Comment on the morphology of the erythrocytes.
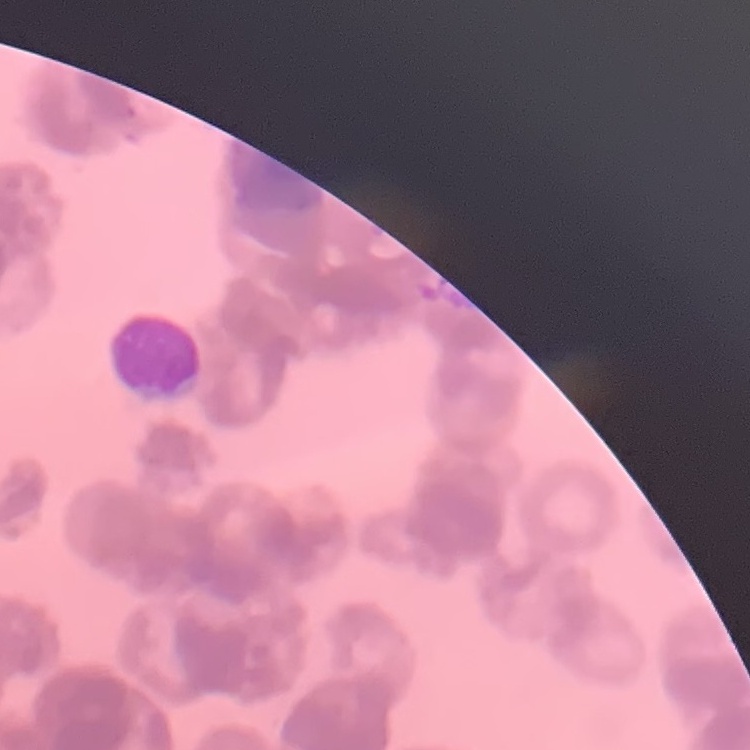
Rouleaux formation.

Square crop of a larger photomicrograph. Stained with either Field's or Giemsa. Thin peripheral smear.